Assess for Plasmodium parasites.
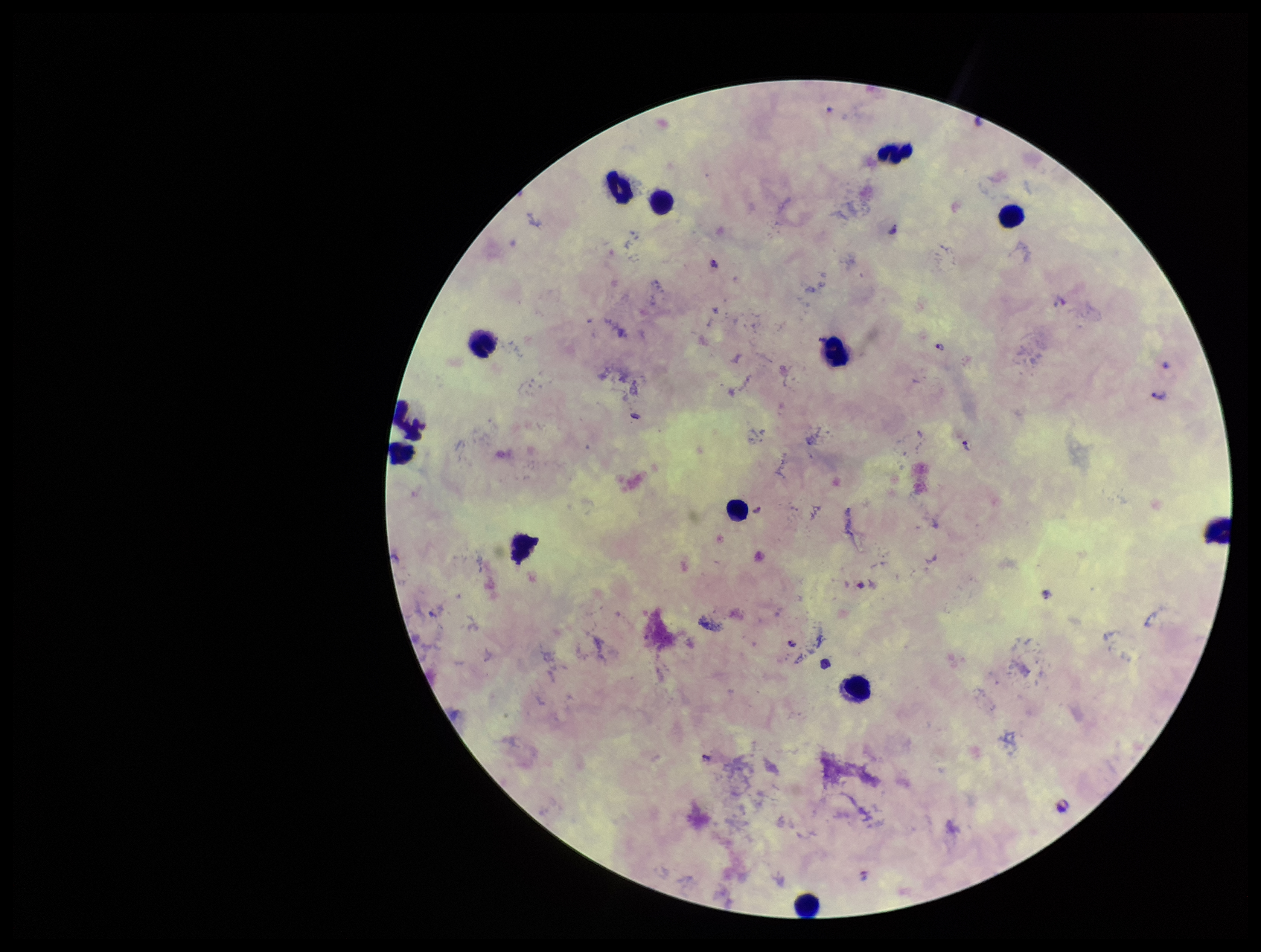
Identified.

capture: smartphone photograph through the microscope eyepiece
field_of_view: one from this slide
preparation: thick smear
parasite_count: 2
leukocyte_count: 13
species_reported_for_this_patient: Plasmodium falciparum
image_size: 1261×952 pixels
stain: Giemsa
patient_malaria_status: infected